Locate every blood parasite and identify its species.
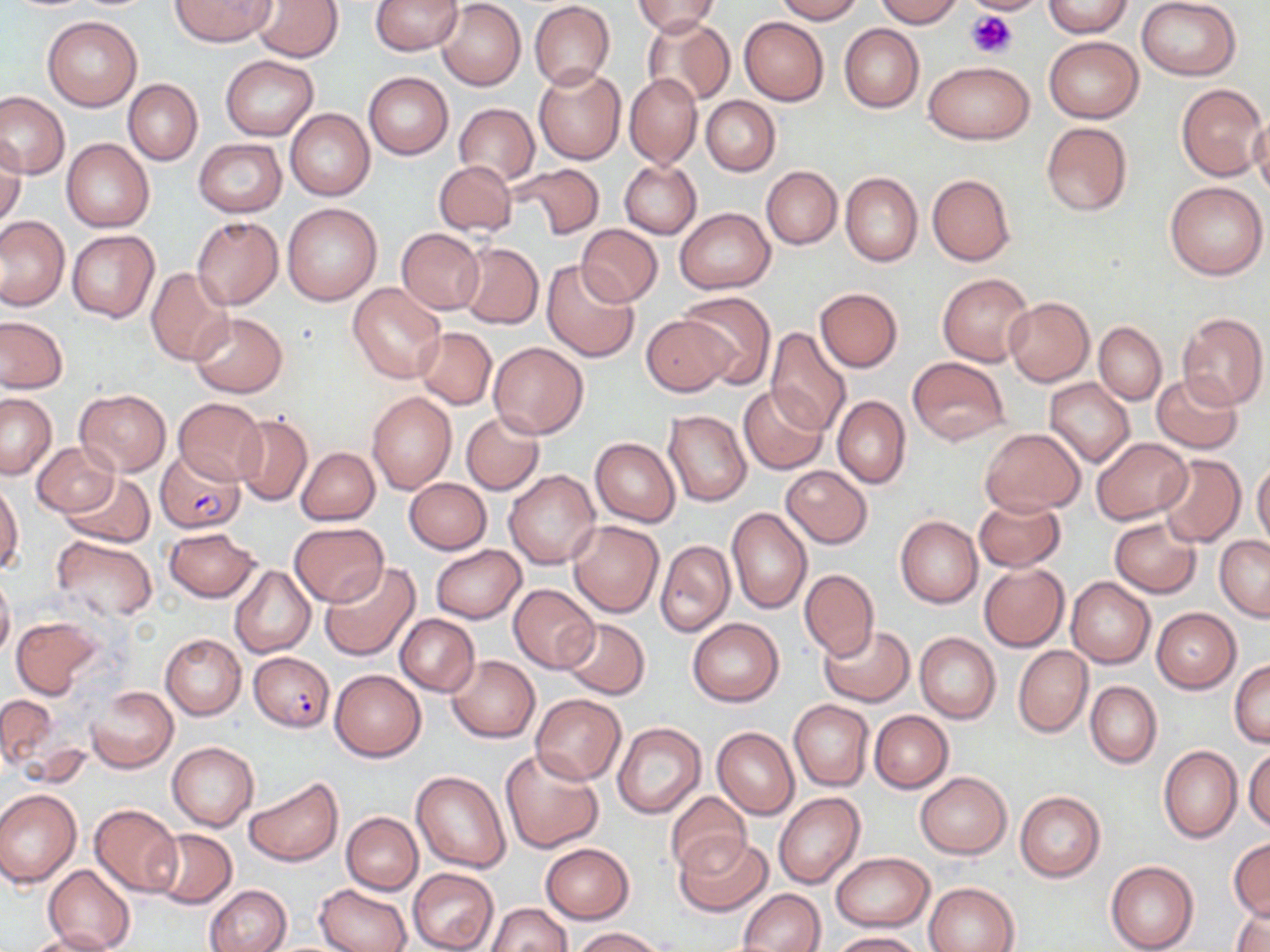

Approximate bounding boxes as (x1, y1, x2, y2) in pixels.
Plasmodium falciparum-infected red blood cells: (155, 449, 244, 532), (248, 652, 334, 731).
No Plasmodium ovale, Plasmodium malariae, Plasmodium vivax, Babesia divergens, or Trypanosoma brucei observed.

Platelet locations: (969, 0, 1039, 14), (966, 10, 1017, 60). Uninfected red blood cell locations: (171, 0, 275, 46), (370, 0, 463, 55), (773, 0, 865, 23), (873, 0, 962, 26), (961, 0, 1049, 14), (1137, 0, 1243, 80), (252, 1, 344, 62), (437, 1, 525, 91), (632, 1, 718, 37), (529, 2, 614, 88), (1042, 2, 1135, 37), (42, 16, 142, 111), (739, 16, 828, 105), (643, 18, 734, 108), (839, 24, 924, 112), (1044, 36, 1144, 122), (220, 55, 318, 138), (922, 61, 1034, 144), (533, 67, 626, 164), (363, 73, 452, 159), (624, 74, 701, 168), (122, 79, 202, 165), (1176, 83, 1269, 181), (0, 90, 69, 180), (701, 96, 780, 176), (454, 103, 539, 186), (285, 109, 375, 200), (1250, 115, 1270, 203), (1040, 120, 1132, 217), (1, 135, 27, 229), (194, 138, 286, 217), (61, 139, 154, 231), (433, 159, 518, 236), (620, 161, 701, 238), (510, 163, 604, 240), (761, 166, 842, 250), (840, 173, 922, 266), (927, 174, 1016, 266), (1164, 180, 1268, 280), (283, 203, 382, 304), (675, 208, 774, 294), (1, 216, 69, 310), (191, 217, 282, 310), (576, 224, 662, 307), (397, 228, 485, 314), (67, 230, 160, 322), (457, 243, 543, 329), (542, 258, 642, 363), (146, 267, 233, 366), (937, 273, 1032, 366), (348, 282, 446, 384), (815, 287, 903, 372), (678, 291, 776, 388), (1004, 297, 1094, 387), (1177, 311, 1268, 410), (189, 312, 287, 397), (641, 314, 733, 395), (0, 315, 67, 393), (1094, 322, 1166, 405), (414, 327, 497, 409), (765, 328, 851, 435), (488, 342, 589, 439), (907, 357, 1010, 445), (1151, 372, 1244, 453), (1044, 377, 1135, 468), (738, 386, 828, 474), (75, 389, 170, 476), (367, 391, 457, 493), (0, 392, 56, 479), (831, 396, 910, 488), (172, 397, 267, 485), (663, 410, 751, 506), (233, 413, 312, 507), (462, 413, 544, 494), (980, 428, 1085, 515), (1091, 437, 1192, 524), (591, 438, 680, 527), (31, 440, 119, 517), (297, 447, 379, 525), (1155, 454, 1246, 547), (1252, 460, 1270, 552), (782, 466, 872, 548), (503, 470, 599, 570), (58, 472, 154, 547), (403, 478, 491, 555), (1, 483, 22, 572), (974, 497, 1066, 571), (727, 508, 811, 613), (896, 516, 982, 608), (1109, 517, 1201, 597), (567, 521, 663, 616), (289, 522, 388, 606), (164, 528, 261, 602), (1215, 535, 1270, 622), (50, 536, 157, 623), (655, 540, 734, 637), (432, 545, 526, 623), (320, 562, 423, 662), (978, 563, 1069, 651), (230, 565, 316, 659), (0, 569, 15, 663), (799, 569, 879, 659), (1067, 578, 1154, 668), (508, 584, 599, 671), (1151, 608, 1239, 692), (394, 614, 479, 696), (11, 616, 106, 698), (687, 617, 784, 706), (559, 618, 651, 700), (817, 624, 915, 705), (914, 632, 1000, 723), (160, 633, 245, 720), (1013, 645, 1091, 737), (446, 654, 540, 742), (1229, 659, 1269, 748), (329, 670, 425, 761), (1085, 681, 1160, 768), (87, 686, 177, 773), (530, 692, 626, 785), (1, 694, 55, 768), (789, 700, 873, 791), (868, 710, 952, 793), (612, 721, 707, 819), (712, 726, 799, 819), (166, 742, 259, 831), (1245, 745, 1270, 831), (1159, 746, 1242, 844), (498, 747, 605, 853), (411, 770, 511, 873), (915, 772, 1011, 858), (244, 777, 342, 867), (0, 787, 81, 887), (1015, 790, 1105, 882), (665, 791, 751, 876), (773, 792, 866, 890), (89, 803, 182, 896), (340, 812, 422, 894), (148, 829, 236, 908), (676, 833, 774, 916), (1228, 838, 1269, 921), (541, 843, 634, 922), (831, 852, 934, 931), (1105, 860, 1199, 952), (43, 865, 135, 952), (407, 868, 499, 952), (925, 882, 1019, 952), (315, 884, 411, 952), (204, 885, 291, 951), (740, 889, 825, 951), (1231, 899, 1270, 952), (487, 902, 571, 952), (572, 927, 664, 951), (22, 930, 120, 952), (830, 931, 927, 952). Slide-level diagnosis: Plasmodium falciparum. Thin blood film. 1000x magnification. May-Grünwald-Giemsa stain. One field of a larger specimen. Optical microscopy. Image is 1270×952 pixels.